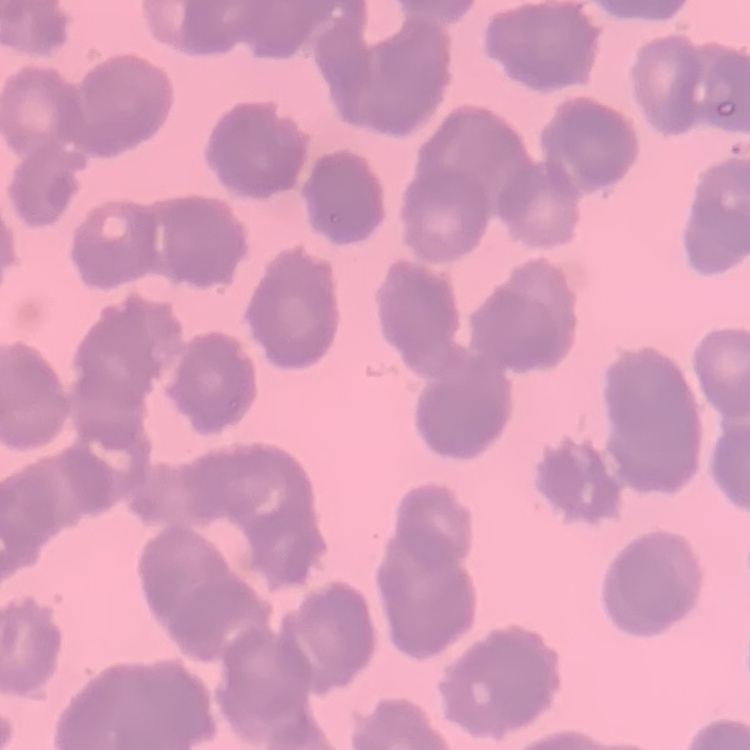

Summary:
  - Erythrocyte morphology: rouleaux formation
  - Preparation: thin peripheral smear
  - Image type: one tile cut from a larger photomicrograph
  - Stain: Field's or Giemsa